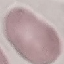
result = no malaria parasites detected
capture = smartphone through the microscope eyepiece
preparation = thin smear
image type = cell patch, automatically extracted from a larger field of view and resized to 64 × 64 pixels
stain = Giemsa